Assess this cell for malaria.
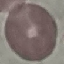
Uninfected.

Summary:
  - Stain: Giemsa
  - Preparation: thin blood film
  - Image type: cell patch, automatically extracted from a larger field of view and resized to 64 × 64 pixels
  - Capture: smartphone camera at the microscope eyepiece